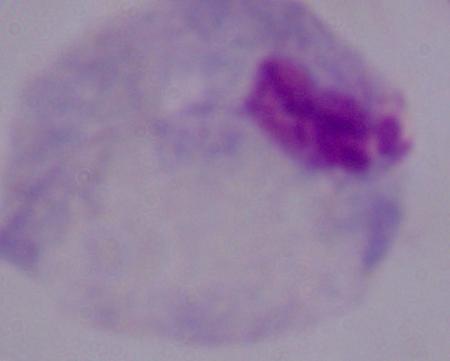

Micrograph. A trichomonad is shown. 1000x magnification.